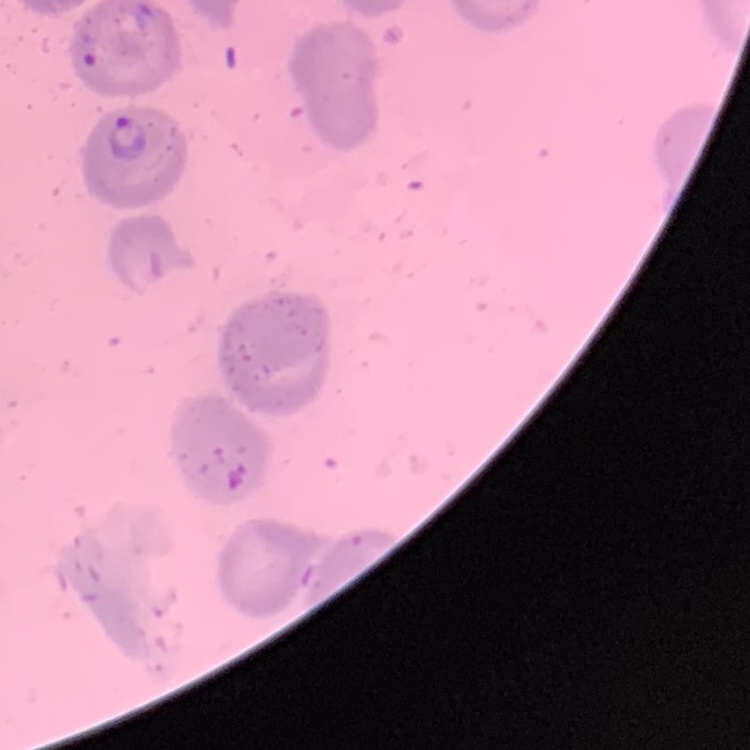

Summary:
  - Red blood cell morphology: no rouleaux formation
  - Image type: square crop of a larger photomicrograph
  - Preparation: thin peripheral smear
  - Stain: Field's or Giemsa